Assess this cell for malaria.
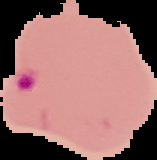

It is parasitized.

Cell region segmented out of the field of view; the surrounding area is masked to black. Image is 157×160 pixels. From a thin blood film.